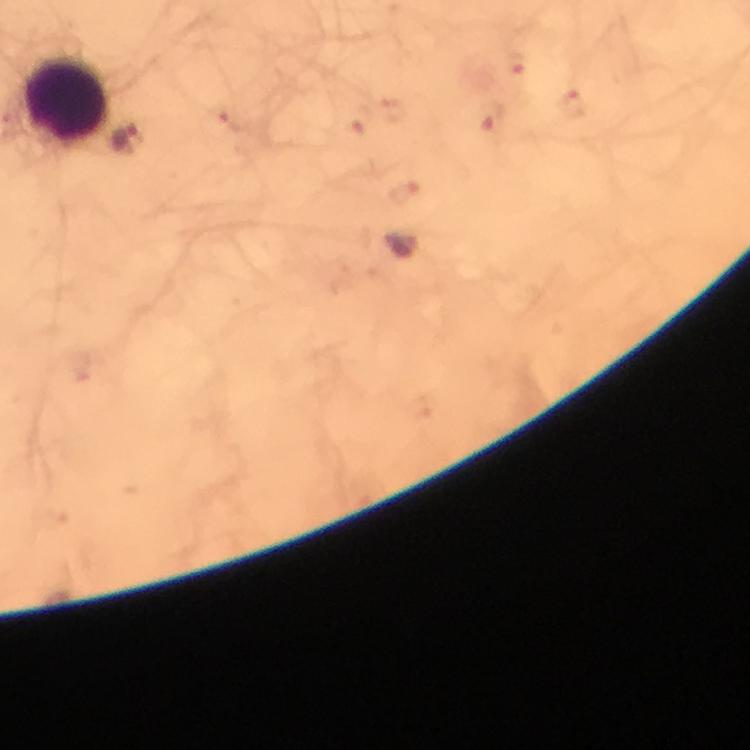
malaria parasite locations = approximate centers as [x, y] in pixels: [517, 65], [573, 100], [359, 120], [495, 127], [128, 140], [407, 195]
image size = 750×750 pixels
cropped from = a single field of view
stain = Giemsa
magnification = 100x
preparation = thick blood film
leukocyte locations = approximate centers as [x, y] in pixels: [67, 100]
immersion oil = used
capture = smartphone photograph through a microscope
context = from a diagnostic examination for malaria